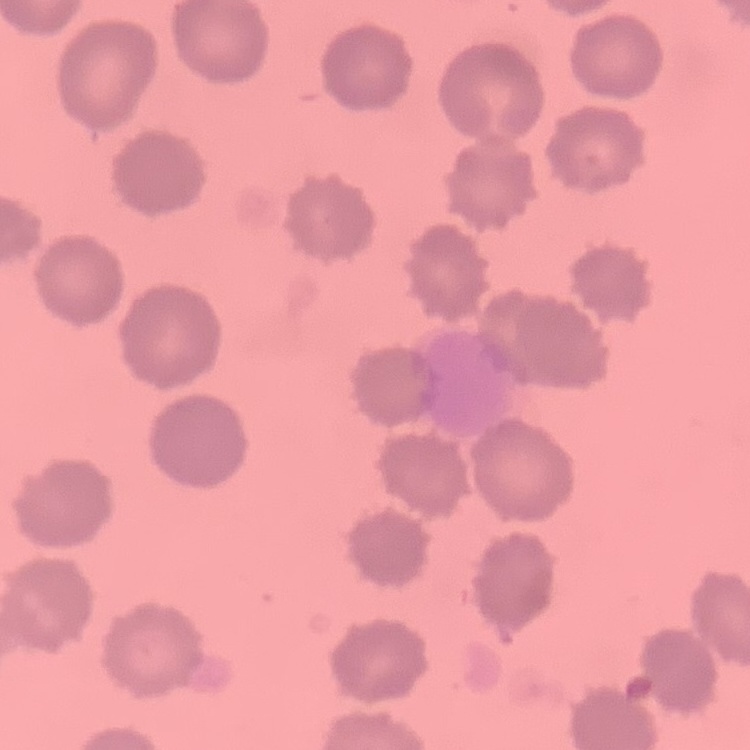

Summary:
  - Red blood cell morphology: no rouleaux formation
  - Image type: square crop of a larger photomicrograph
  - Stain: Field's or Giemsa
  - Preparation: thin blood smear